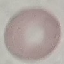

{
  "malaria_status": "uninfected",
  "image_type": "cell patch, automatically extracted from a larger field of view and resized to 64 × 64 pixels",
  "capture": "smartphone through the microscope eyepiece",
  "preparation": "thin blood smear",
  "stain": "Giemsa"
}